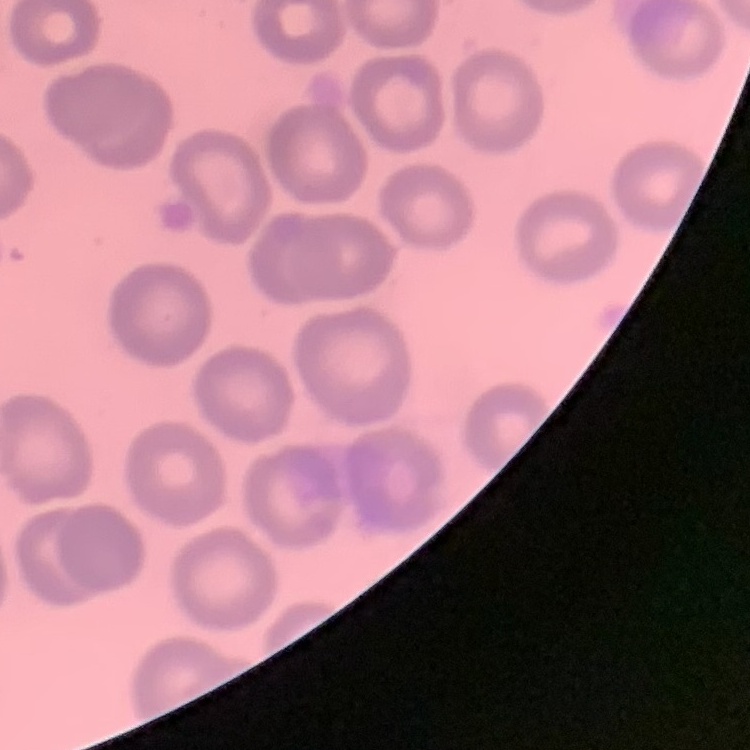
erythrocyte morphology = no rouleaux formation
preparation = thin blood film
image type = square crop of a larger photomicrograph
stain = Field's or Giemsa